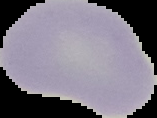 From a thin blood film. Result: negative for malaria parasites. Segmented cell region on a black background. Image is 157×118 pixels.